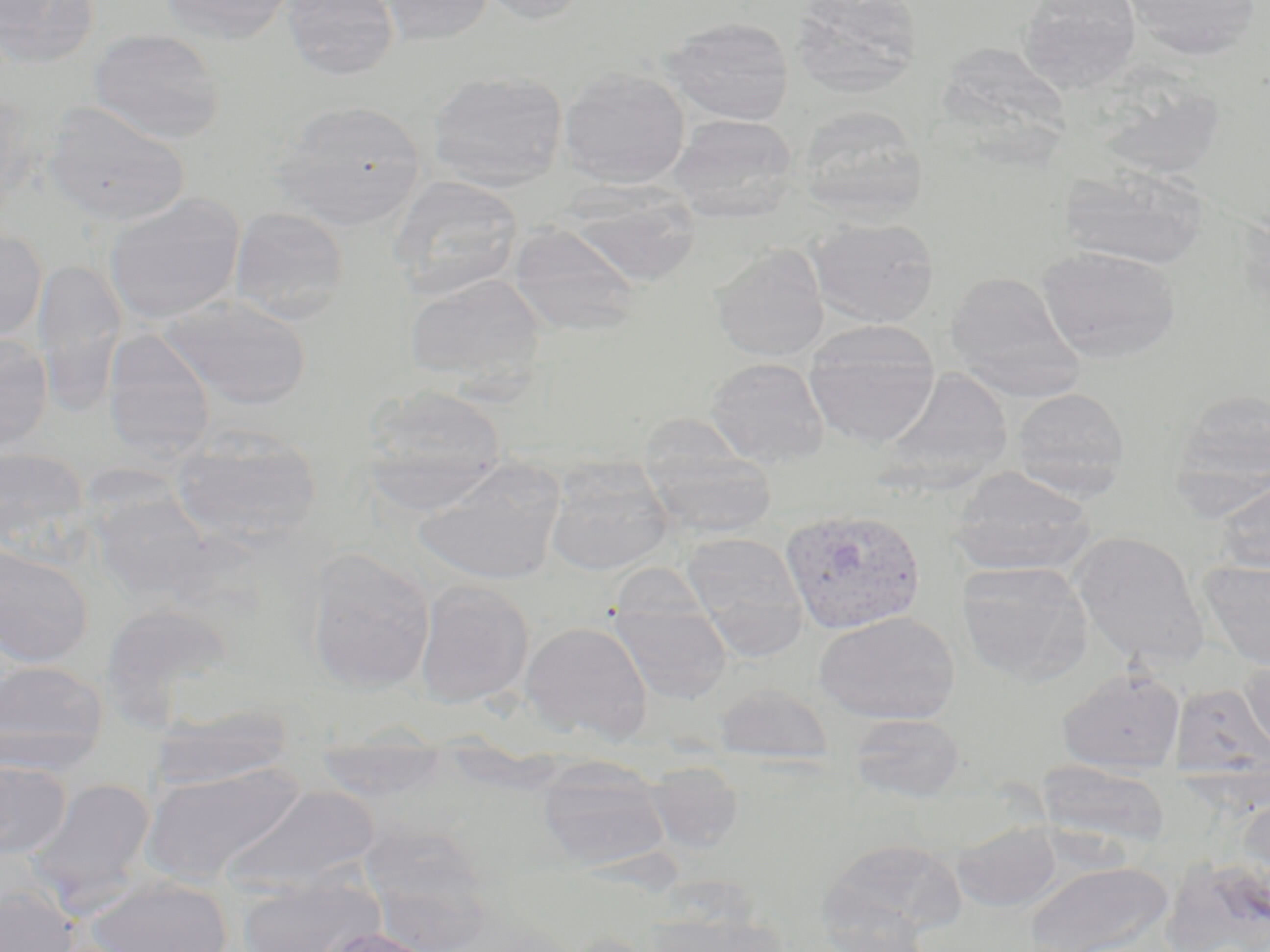

slide-level diagnosis = Plasmodium vivax
magnification = 1000x
preparation = thin blood smear
modality = optical microscopy
image size = 1270×952 pixels
stain = May-Grünwald-Giemsa
field of view = single
uninfected red blood cell locations = approximate bounding boxes as (x1,y1)-(x2,y2) corner pairs in pixels: (1,0)-(101,68), (158,0)-(295,46), (281,0)-(399,80), (376,0)-(495,46), (476,0)-(590,25), (790,0)-(924,97), (1120,0)-(1263,61), (1017,1)-(1141,92), (660,16)-(795,125), (88,28)-(226,144), (558,67)-(691,189), (426,70)-(569,191), (1090,71)-(1228,182), (0,89)-(36,222), (268,99)-(427,229), (41,101)-(191,228), (794,105)-(929,221), (669,114)-(799,222), (1058,165)-(1211,270), (387,176)-(524,301), (560,182)-(702,287), (103,193)-(247,325), (229,207)-(350,324), (808,218)-(939,328), (508,222)-(642,336), (0,226)-(48,345), (711,244)-(829,362), (1035,245)-(1182,364), (34,258)-(126,416), (945,271)-(1085,399), (404,273)-(547,393), (157,294)-(312,410), (804,323)-(941,447), (102,328)-(216,463), (0,333)-(53,452), (705,357)-(830,468), (875,367)-(1016,491), (362,384)-(508,504), (1010,387)-(1130,496), (1171,387)-(1270,500), (170,427)-(323,546), (641,444)-(777,538), (0,447)-(92,558), (543,459)-(675,576), (414,461)-(564,586), (947,467)-(1097,576), (1211,473)-(1270,575), (83,481)-(217,604), (1071,531)-(1208,667), (680,532)-(809,658), (0,544)-(94,667), (304,548)-(436,693), (1198,560)-(1270,670), (956,561)-(1093,686), (414,580)-(535,708), (609,598)-(732,706), (98,602)-(236,719), (814,610)-(960,724), (520,620)-(652,742), (1240,657)-(1270,763), (0,660)-(108,776), (1057,667)-(1186,773), (1171,683)-(1269,782), (712,684)-(834,765), (150,704)-(294,791), (848,713)-(967,803), (314,738)-(450,802), (537,757)-(670,871), (0,759)-(72,860), (644,760)-(743,854), (1035,760)-(1172,852), (141,762)-(308,885), (23,777)-(157,912), (220,785)-(381,896), (1236,793)-(1270,901), (950,819)-(1064,913), (362,836)-(496,948), (823,837)-(966,937), (1160,855)-(1270,952), (1023,861)-(1173,952), (235,873)-(385,952), (83,877)-(235,952), (0,885)-(80,952), (814,889)-(934,952), (643,908)-(788,952), (310,926)-(445,952)
Plasmodium vivax-infected red blood cell locations = approximate bounding boxes as (x1,y1)-(x2,y2) corner pairs in pixels: (780,506)-(926,635)